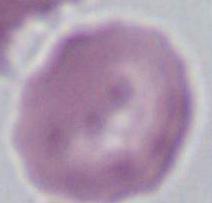

modality = micrograph
identification = erythrocyte
magnification = 1000x